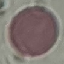

Summary:
  - Malaria status: uninfected
  - Stain: Giemsa
  - Preparation: thin blood film
  - Image type: cell patch, automatically extracted from a larger field of view and resized to 64 × 64 pixels
  - Capture: smartphone camera at the microscope eyepiece